Describe the morphology of the red blood cells.
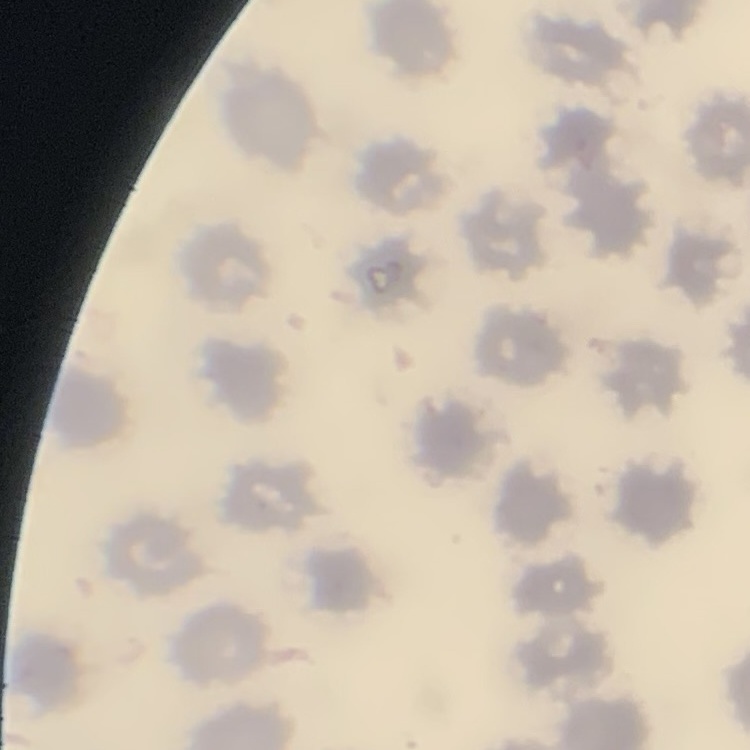

No rouleaux formation.

Summary:
  - Image type: one tile cut from a larger photomicrograph
  - Stain: Field's or Giemsa
  - Preparation: thin blood smear